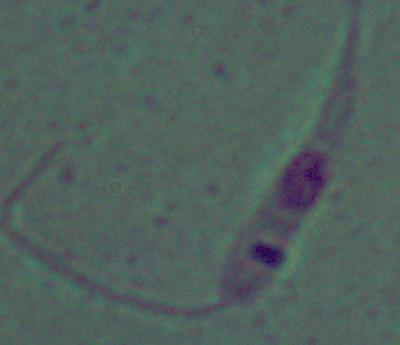
Summary:
  - Modality: micrograph
  - Magnification: 1000x
  - Identification: Leishmania